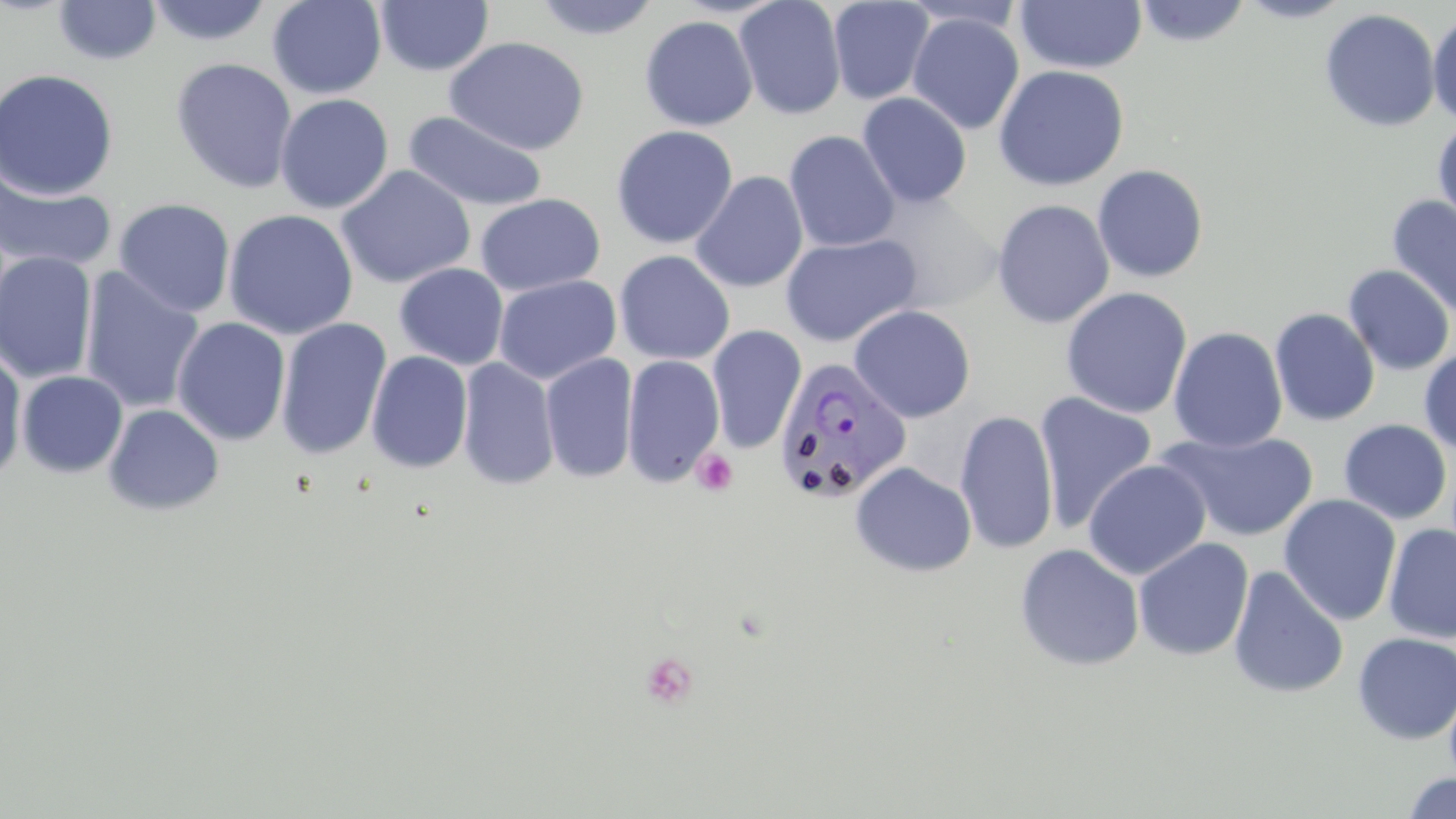

{
  "slide_level_diagnosis": "Plasmodium vivax",
  "magnification": "1000x",
  "uninfected_red_blood_cell_locations": "approximate bounding boxes as (x1, y1, x2, y2) in pixels: (145, 0, 274, 47), (267, 0, 387, 99), (530, 0, 661, 40), (733, 0, 847, 120), (1015, 0, 1146, 73), (1235, 0, 1355, 23), (53, 1, 162, 65), (375, 1, 494, 76), (827, 1, 934, 105), (1133, 1, 1253, 48), (894, 2, 1032, 34), (1319, 8, 1441, 132), (1427, 11, 1456, 127), (907, 12, 1024, 135), (639, 15, 758, 131), (444, 37, 589, 156), (171, 57, 298, 194), (993, 64, 1129, 191), (0, 68, 119, 200), (857, 92, 972, 208), (274, 93, 395, 214), (402, 110, 549, 213), (1432, 118, 1456, 232), (610, 125, 738, 249), (784, 130, 900, 252), (1092, 164, 1209, 284), (336, 165, 475, 289), (0, 170, 117, 275), (690, 171, 808, 293), (872, 192, 1002, 312), (475, 193, 605, 296), (1386, 195, 1456, 321), (113, 198, 236, 318), (991, 199, 1114, 329), (223, 208, 359, 340), (780, 234, 920, 347), (614, 250, 735, 365), (0, 251, 98, 385), (394, 262, 509, 369), (1342, 264, 1455, 376), (80, 267, 205, 414), (494, 275, 621, 385), (1060, 287, 1193, 418), (848, 305, 976, 423), (1269, 308, 1380, 426), (171, 316, 291, 446), (275, 317, 392, 460), (706, 325, 807, 454), (1168, 326, 1287, 453), (1418, 346, 1456, 455), (0, 347, 28, 486), (366, 350, 474, 474), (540, 351, 639, 484), (622, 354, 725, 488), (456, 357, 559, 491), (16, 370, 128, 478), (1034, 392, 1158, 534), (103, 403, 225, 516), (955, 410, 1059, 555), (1338, 419, 1452, 524), (1161, 431, 1320, 542), (1083, 458, 1211, 581), (850, 462, 976, 577), (1279, 494, 1402, 625), (1382, 523, 1456, 643), (1133, 537, 1254, 662), (1014, 543, 1145, 671), (1228, 565, 1349, 699), (1352, 631, 1456, 745), (1400, 771, 1456, 818)",
  "stain": "May-Grünwald-Giemsa",
  "platelet_locations": "approximate bounding boxes as (x1, y1, x2, y2) in pixels: (690, 449, 738, 496), (640, 652, 700, 710)",
  "image_size": "1456×819 pixels",
  "field_of_view": "one of a larger specimen",
  "plasmodium_vivax_infected_red_blood_cell_locations": "approximate bounding boxes as (x1, y1, x2, y2) in pixels: (772, 357, 912, 503)",
  "modality": "optical microscopy",
  "preparation": "thin blood film"
}